State the blood parasite species.
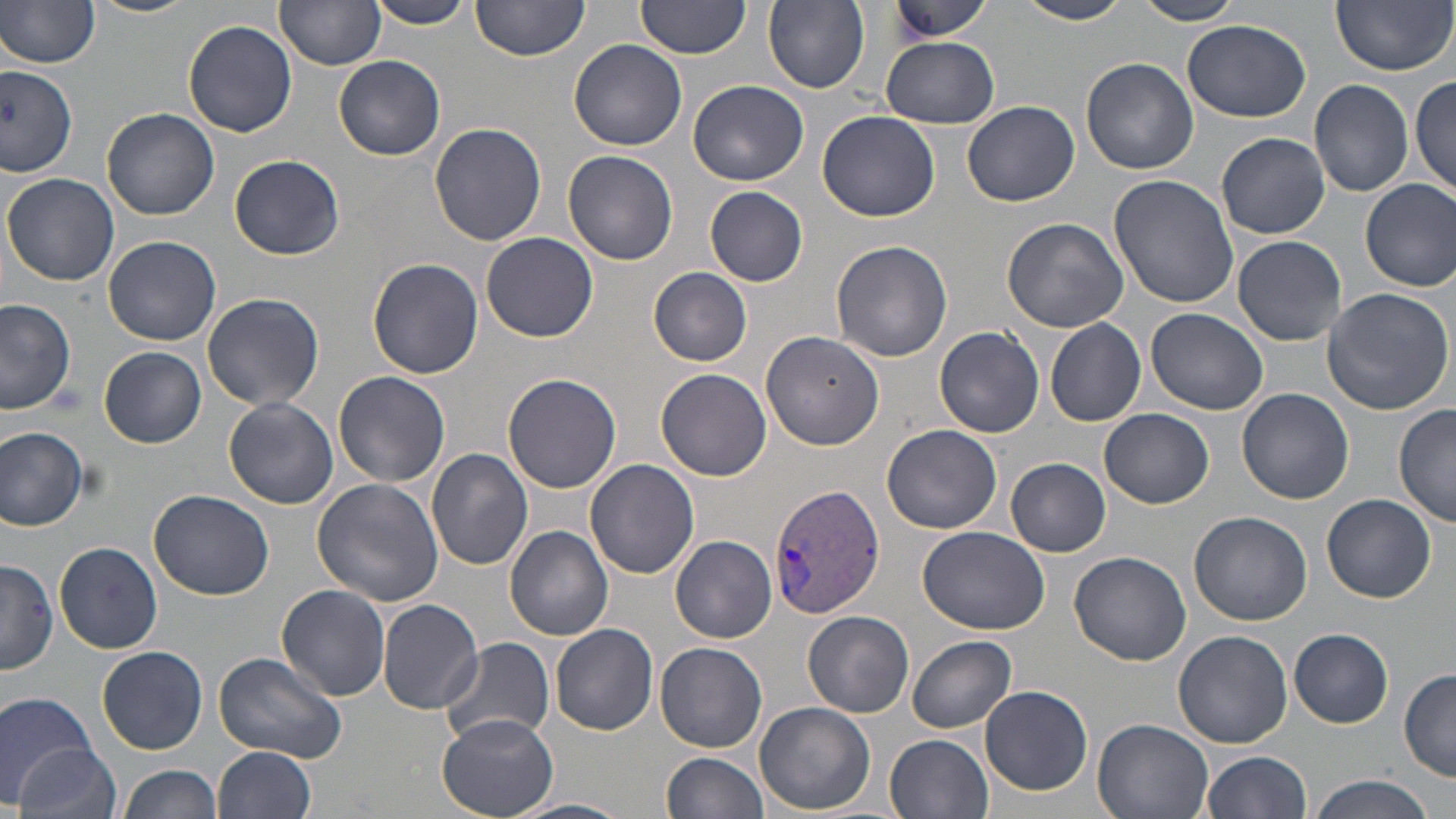

Plasmodium vivax.

Summary:
  - Coordinate format: approximate bounding boxes as [x1, y1, x2, y2] in pixels
  - Uninfected red blood cell locations: [1, 0, 100, 69], [85, 0, 198, 18], [472, 0, 589, 61], [636, 0, 752, 60], [764, 0, 869, 93], [889, 0, 996, 42], [1018, 0, 1132, 25], [1132, 0, 1247, 24], [1332, 0, 1453, 75], [366, 1, 473, 29], [279, 2, 385, 70], [183, 18, 298, 138], [1182, 19, 1310, 123], [880, 36, 999, 128], [570, 38, 687, 150], [334, 55, 445, 160], [1079, 57, 1198, 174], [0, 68, 77, 179], [1411, 74, 1456, 195], [689, 79, 809, 185], [1309, 80, 1414, 197], [962, 101, 1079, 207], [101, 106, 219, 221], [819, 111, 939, 221], [429, 122, 546, 247], [1215, 132, 1331, 239], [563, 149, 678, 266], [230, 153, 345, 260], [1109, 172, 1241, 308], [3, 174, 121, 287], [1360, 179, 1456, 292], [705, 186, 808, 286], [1001, 215, 1130, 334], [482, 232, 598, 343], [102, 235, 220, 347], [1232, 235, 1348, 346], [831, 239, 951, 362], [368, 259, 484, 379], [647, 266, 752, 367], [1321, 287, 1454, 414], [202, 291, 325, 411], [0, 298, 77, 416], [1147, 308, 1268, 416], [1044, 319, 1146, 426], [934, 325, 1046, 437], [761, 331, 885, 450], [98, 347, 207, 448], [657, 367, 771, 481], [334, 372, 450, 490], [502, 372, 623, 495], [1237, 388, 1355, 505], [223, 398, 338, 507], [1393, 404, 1455, 529], [1101, 408, 1213, 506], [882, 423, 1002, 533], [0, 426, 92, 530], [426, 447, 533, 571], [1006, 458, 1111, 557], [585, 459, 701, 580], [310, 478, 444, 607], [150, 489, 274, 600], [1322, 494, 1435, 602], [1188, 510, 1311, 625], [505, 525, 615, 641], [917, 526, 1051, 636], [670, 535, 776, 643], [54, 542, 163, 655], [1069, 550, 1192, 666], [1, 559, 57, 673], [277, 582, 391, 703], [377, 599, 482, 714], [803, 612, 914, 718], [551, 623, 659, 735], [1289, 629, 1392, 727], [1173, 630, 1293, 748], [439, 636, 555, 747], [908, 636, 1017, 733], [654, 642, 768, 752], [97, 646, 208, 754], [214, 650, 348, 764], [1398, 668, 1456, 782], [981, 685, 1093, 796], [0, 691, 101, 806], [755, 702, 875, 814], [438, 714, 558, 817], [1092, 718, 1215, 819], [886, 733, 993, 818], [13, 742, 121, 819], [213, 746, 317, 818], [1201, 750, 1314, 818], [660, 752, 768, 819], [119, 764, 222, 819], [1307, 775, 1438, 819], [510, 798, 631, 819]
  - Plasmodium vivax-infected red blood cell locations: [767, 484, 884, 619]
  - Image size: 1456×819 pixels
  - Stain: May-Grünwald-Giemsa
  - Modality: optical microscopy
  - Preparation: thin blood film
  - Magnification: 1000x
  - Field of view: single